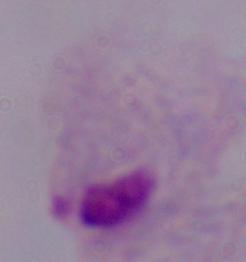
Summary:
  - Modality: photomicrograph
  - Magnification: 1000x
  - Identification: trichomonad